Outline each Plasmodium malariae-infected red blood cell.
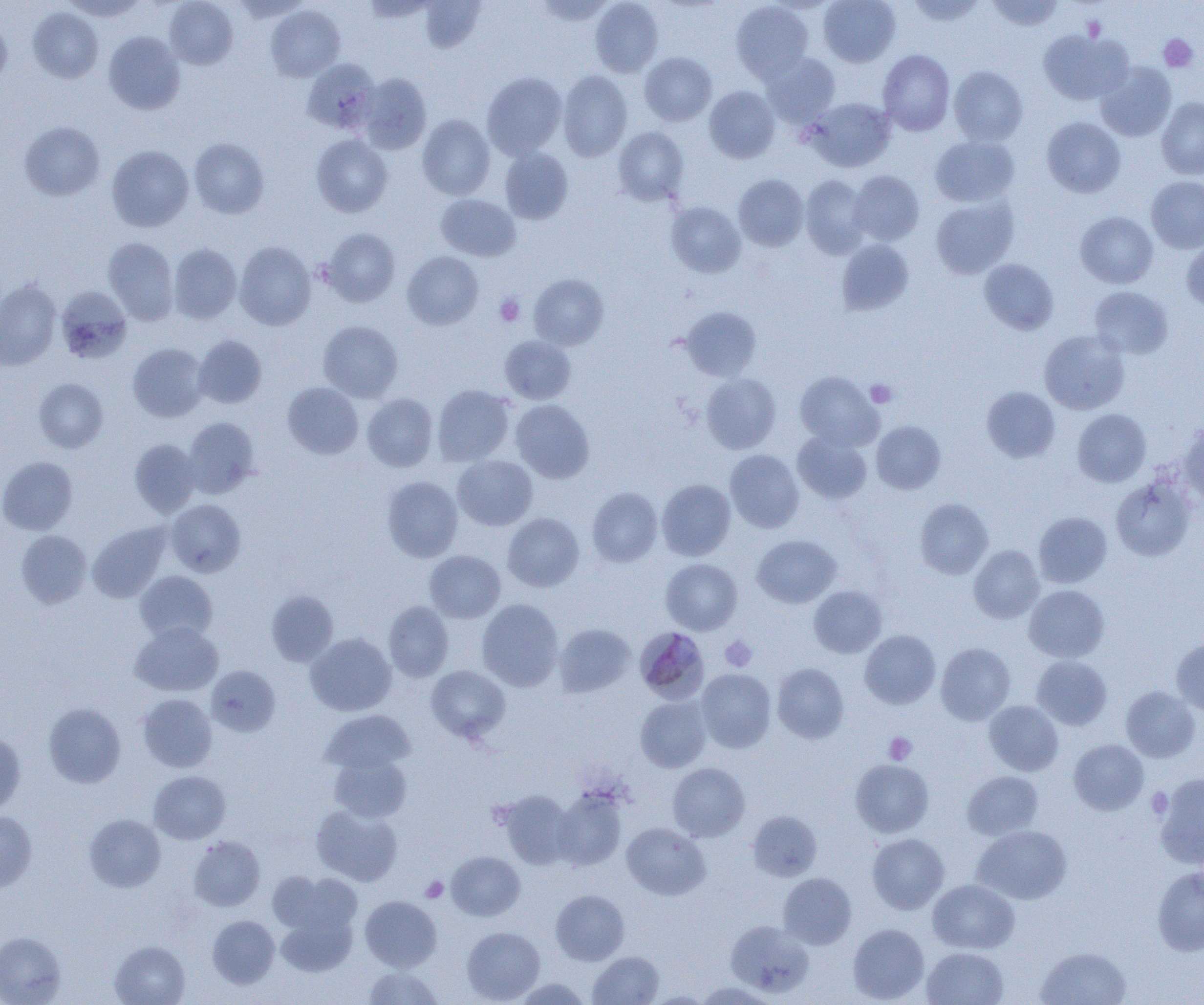

Approximate bounding boxes as named x1/y1/x2/y2 corners in pixels.
Plasmodium malariae-infected red blood cells: (x1=640, y1=629, x2=713, y2=703).

Summary:
  - Uninfected red blood cell locations: (x1=61, y1=0, x2=148, y2=21), (x1=164, y1=0, x2=238, y2=69), (x1=360, y1=0, x2=438, y2=22), (x1=534, y1=0, x2=615, y2=25), (x1=590, y1=0, x2=664, y2=77), (x1=818, y1=0, x2=901, y2=67), (x1=904, y1=0, x2=987, y2=26), (x1=986, y1=0, x2=1065, y2=31), (x1=417, y1=1, x2=486, y2=53), (x1=730, y1=1, x2=814, y2=82), (x1=265, y1=5, x2=345, y2=81), (x1=27, y1=7, x2=103, y2=83), (x1=0, y1=18, x2=12, y2=88), (x1=1038, y1=29, x2=1133, y2=105), (x1=103, y1=31, x2=185, y2=114), (x1=878, y1=49, x2=955, y2=135), (x1=639, y1=52, x2=717, y2=126), (x1=760, y1=52, x2=841, y2=127), (x1=302, y1=58, x2=380, y2=134), (x1=1095, y1=61, x2=1176, y2=142), (x1=948, y1=65, x2=1028, y2=145), (x1=558, y1=70, x2=633, y2=162), (x1=356, y1=72, x2=432, y2=154), (x1=482, y1=72, x2=567, y2=159), (x1=704, y1=86, x2=780, y2=163), (x1=1156, y1=97, x2=1204, y2=179), (x1=804, y1=98, x2=895, y2=172), (x1=417, y1=114, x2=495, y2=200), (x1=1041, y1=117, x2=1125, y2=198), (x1=19, y1=121, x2=105, y2=201), (x1=613, y1=126, x2=689, y2=206), (x1=311, y1=134, x2=393, y2=217), (x1=930, y1=134, x2=1019, y2=207), (x1=188, y1=137, x2=270, y2=219), (x1=106, y1=145, x2=194, y2=232), (x1=499, y1=147, x2=573, y2=224), (x1=848, y1=170, x2=924, y2=246), (x1=733, y1=174, x2=810, y2=251), (x1=800, y1=175, x2=871, y2=258), (x1=1146, y1=176, x2=1204, y2=254), (x1=436, y1=194, x2=520, y2=261), (x1=930, y1=196, x2=1018, y2=279), (x1=665, y1=201, x2=746, y2=278), (x1=1075, y1=211, x2=1158, y2=288), (x1=319, y1=228, x2=400, y2=307), (x1=103, y1=238, x2=179, y2=325), (x1=836, y1=239, x2=914, y2=315), (x1=1182, y1=240, x2=1204, y2=312), (x1=234, y1=241, x2=316, y2=330), (x1=168, y1=243, x2=242, y2=324), (x1=402, y1=251, x2=483, y2=329), (x1=978, y1=258, x2=1059, y2=335), (x1=529, y1=273, x2=608, y2=350), (x1=0, y1=280, x2=62, y2=370), (x1=1089, y1=286, x2=1173, y2=359), (x1=56, y1=287, x2=132, y2=364), (x1=679, y1=306, x2=762, y2=381), (x1=318, y1=320, x2=403, y2=402), (x1=1039, y1=329, x2=1130, y2=415), (x1=194, y1=335, x2=267, y2=408), (x1=500, y1=335, x2=576, y2=404), (x1=128, y1=343, x2=208, y2=422), (x1=795, y1=371, x2=883, y2=450), (x1=700, y1=373, x2=781, y2=454), (x1=34, y1=377, x2=108, y2=453), (x1=282, y1=382, x2=363, y2=459), (x1=432, y1=384, x2=515, y2=467), (x1=981, y1=386, x2=1060, y2=463), (x1=362, y1=393, x2=438, y2=472), (x1=511, y1=399, x2=595, y2=484), (x1=1072, y1=409, x2=1151, y2=487), (x1=183, y1=417, x2=261, y2=498), (x1=871, y1=421, x2=946, y2=494), (x1=1179, y1=422, x2=1204, y2=508), (x1=792, y1=430, x2=872, y2=504), (x1=129, y1=438, x2=201, y2=518), (x1=725, y1=449, x2=805, y2=533), (x1=452, y1=455, x2=537, y2=531), (x1=0, y1=456, x2=78, y2=535), (x1=382, y1=476, x2=463, y2=562), (x1=1110, y1=477, x2=1195, y2=561), (x1=657, y1=479, x2=735, y2=560), (x1=587, y1=487, x2=663, y2=567), (x1=915, y1=498, x2=993, y2=579), (x1=165, y1=499, x2=246, y2=577), (x1=1033, y1=511, x2=1112, y2=588), (x1=502, y1=513, x2=584, y2=592), (x1=88, y1=523, x2=170, y2=603), (x1=15, y1=530, x2=92, y2=609), (x1=752, y1=535, x2=841, y2=608), (x1=969, y1=545, x2=1044, y2=623), (x1=424, y1=550, x2=505, y2=623), (x1=660, y1=558, x2=742, y2=635), (x1=134, y1=570, x2=217, y2=643), (x1=808, y1=585, x2=887, y2=658), (x1=1024, y1=585, x2=1109, y2=662), (x1=266, y1=590, x2=339, y2=666), (x1=477, y1=599, x2=564, y2=691), (x1=383, y1=601, x2=454, y2=682), (x1=130, y1=622, x2=223, y2=696), (x1=554, y1=623, x2=636, y2=698), (x1=860, y1=630, x2=940, y2=709), (x1=305, y1=633, x2=396, y2=716), (x1=1170, y1=638, x2=1204, y2=716), (x1=936, y1=642, x2=1015, y2=725), (x1=1032, y1=655, x2=1112, y2=730), (x1=772, y1=662, x2=849, y2=743), (x1=206, y1=665, x2=281, y2=737), (x1=426, y1=665, x2=510, y2=743), (x1=696, y1=668, x2=776, y2=753), (x1=1120, y1=686, x2=1200, y2=763), (x1=137, y1=693, x2=217, y2=772), (x1=635, y1=695, x2=712, y2=772), (x1=983, y1=700, x2=1063, y2=776), (x1=44, y1=703, x2=125, y2=787), (x1=320, y1=710, x2=414, y2=775), (x1=0, y1=732, x2=25, y2=816), (x1=1069, y1=739, x2=1149, y2=815), (x1=328, y1=753, x2=412, y2=823), (x1=850, y1=759, x2=935, y2=837), (x1=668, y1=762, x2=750, y2=841), (x1=149, y1=771, x2=230, y2=844), (x1=962, y1=771, x2=1044, y2=839), (x1=1154, y1=773, x2=1204, y2=869), (x1=495, y1=789, x2=576, y2=870), (x1=552, y1=789, x2=627, y2=871), (x1=311, y1=804, x2=403, y2=886), (x1=747, y1=810, x2=822, y2=881), (x1=0, y1=812, x2=37, y2=892), (x1=84, y1=814, x2=165, y2=892), (x1=621, y1=822, x2=710, y2=900), (x1=972, y1=825, x2=1071, y2=904), (x1=867, y1=833, x2=950, y2=914), (x1=188, y1=836, x2=265, y2=911), (x1=446, y1=851, x2=525, y2=920), (x1=1152, y1=865, x2=1204, y2=956), (x1=269, y1=871, x2=362, y2=936), (x1=778, y1=872, x2=856, y2=949), (x1=928, y1=879, x2=1019, y2=953), (x1=551, y1=889, x2=630, y2=965), (x1=360, y1=895, x2=442, y2=971), (x1=276, y1=911, x2=356, y2=977), (x1=207, y1=915, x2=280, y2=988), (x1=725, y1=921, x2=813, y2=997), (x1=848, y1=923, x2=929, y2=1004), (x1=462, y1=926, x2=545, y2=1003), (x1=0, y1=932, x2=66, y2=1004), (x1=110, y1=940, x2=190, y2=1005), (x1=1035, y1=945, x2=1132, y2=1005), (x1=922, y1=947, x2=1009, y2=1005), (x1=588, y1=951, x2=664, y2=1004), (x1=363, y1=967, x2=442, y2=1004), (x1=513, y1=978, x2=591, y2=1005), (x1=695, y1=981, x2=779, y2=1004)
  - Platelet locations: (x1=1158, y1=34, x2=1198, y2=73), (x1=495, y1=294, x2=525, y2=326), (x1=865, y1=380, x2=897, y2=407), (x1=720, y1=635, x2=757, y2=672), (x1=884, y1=732, x2=917, y2=764), (x1=1146, y1=786, x2=1173, y2=819), (x1=421, y1=876, x2=448, y2=902)
  - Slide-level diagnosis: Plasmodium malariae
  - Field of view: one of a larger specimen
  - Image size: 1204×1005 pixels
  - Magnification: 1000x
  - Modality: optical microscopy
  - Preparation: thin blood smear